Outline each Plasmodium ovale-infected red blood cell.
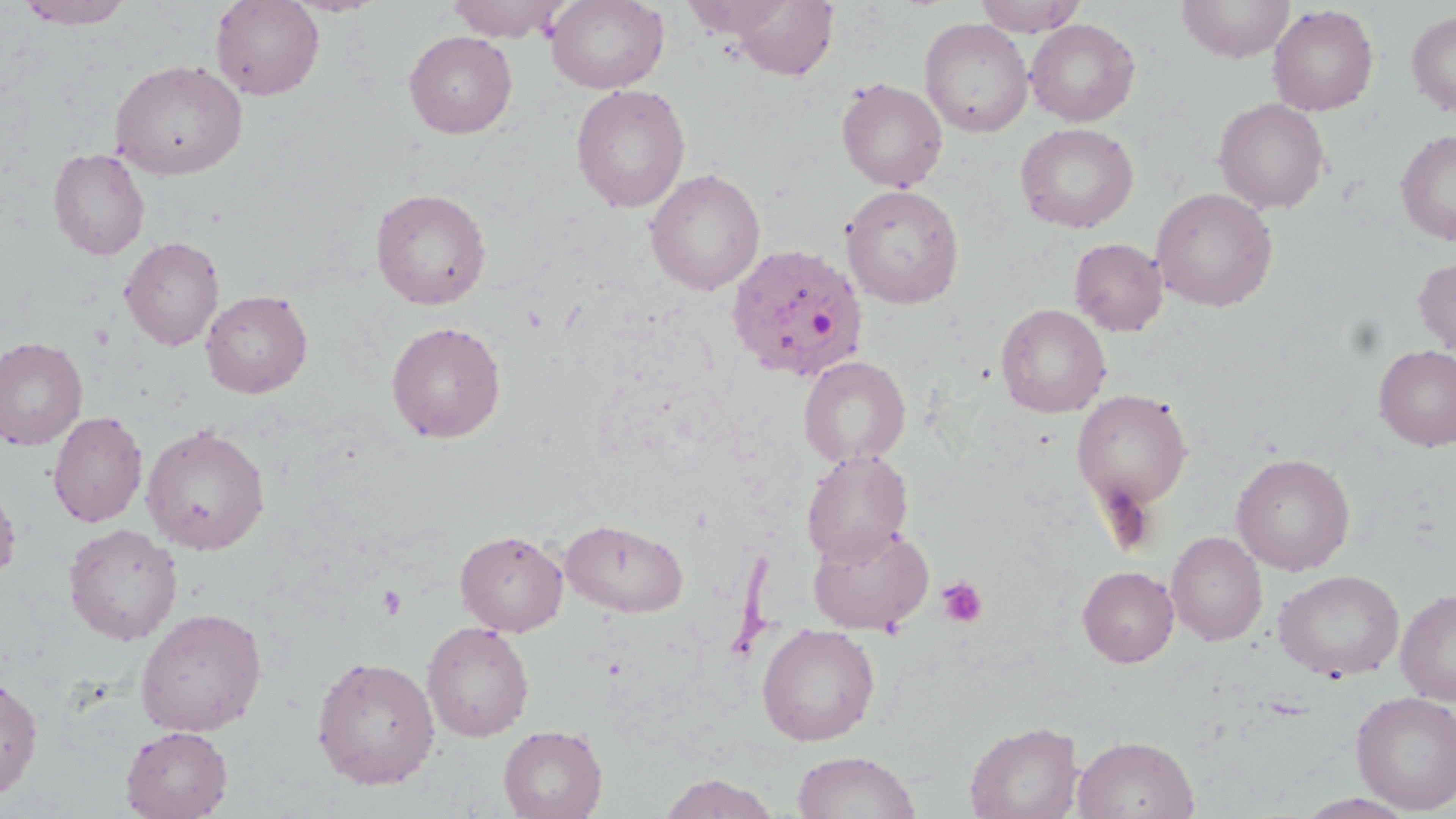

Approximate bounding boxes as [x1, y1, x2, y2] in pixels.
Plasmodium ovale-infected red blood cells: [725, 243, 869, 382].

Summary:
  - Platelet locations: [936, 575, 989, 628], [378, 585, 406, 620]
  - Uninfected red blood cell locations: [13, 0, 136, 29], [210, 0, 325, 101], [283, 0, 388, 17], [445, 0, 569, 42], [545, 0, 669, 93], [683, 0, 796, 39], [729, 0, 839, 80], [972, 0, 1088, 36], [1178, 0, 1294, 62], [1268, 5, 1379, 116], [1406, 10, 1456, 117], [920, 18, 1033, 138], [1025, 19, 1140, 126], [404, 31, 517, 138], [109, 58, 248, 180], [837, 78, 947, 192], [570, 83, 691, 214], [1214, 97, 1330, 215], [1015, 122, 1139, 233], [1396, 129, 1456, 246], [48, 147, 149, 260], [645, 167, 765, 296], [841, 184, 965, 309], [370, 187, 491, 309], [1151, 187, 1278, 312], [120, 236, 224, 351], [1070, 238, 1167, 336], [1413, 256, 1456, 358], [200, 290, 313, 398], [996, 303, 1111, 418], [387, 320, 506, 443], [0, 336, 88, 451], [1373, 344, 1456, 452], [799, 355, 911, 468], [1072, 389, 1193, 512], [47, 410, 147, 528], [141, 423, 271, 555], [801, 449, 914, 566], [1231, 452, 1355, 575], [0, 479, 21, 586], [560, 518, 689, 618], [808, 522, 933, 634], [63, 523, 183, 646], [455, 529, 568, 636], [1167, 531, 1267, 646], [1078, 566, 1179, 667], [1274, 569, 1404, 681], [1396, 588, 1456, 704], [134, 606, 267, 736], [422, 620, 534, 741], [757, 623, 880, 745], [311, 655, 440, 790], [0, 674, 43, 801], [1351, 691, 1456, 813], [965, 721, 1082, 819], [120, 725, 233, 819], [498, 725, 607, 819], [1072, 735, 1199, 819], [791, 750, 921, 819], [656, 774, 782, 818]
  - Slide-level diagnosis: Plasmodium ovale
  - Image size: 1456×819 pixels
  - Stain: May-Grünwald-Giemsa
  - Modality: optical microscopy
  - Magnification: 1000x
  - Preparation: thin blood smear
  - Field of view: single